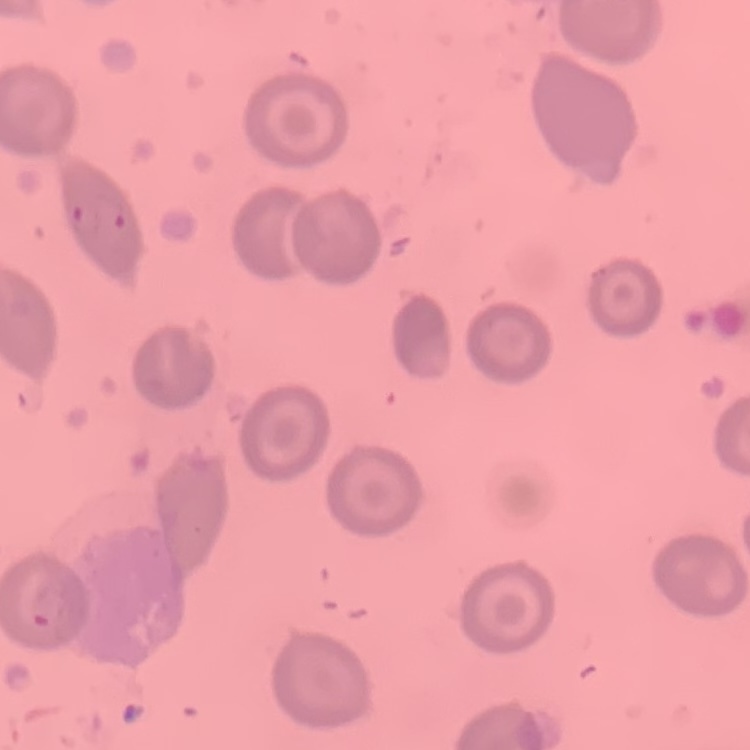
The red blood cells exhibit no rouleaux formation. Field's or Giemsa stain. Square crop of a larger photomicrograph. Thin peripheral smear.